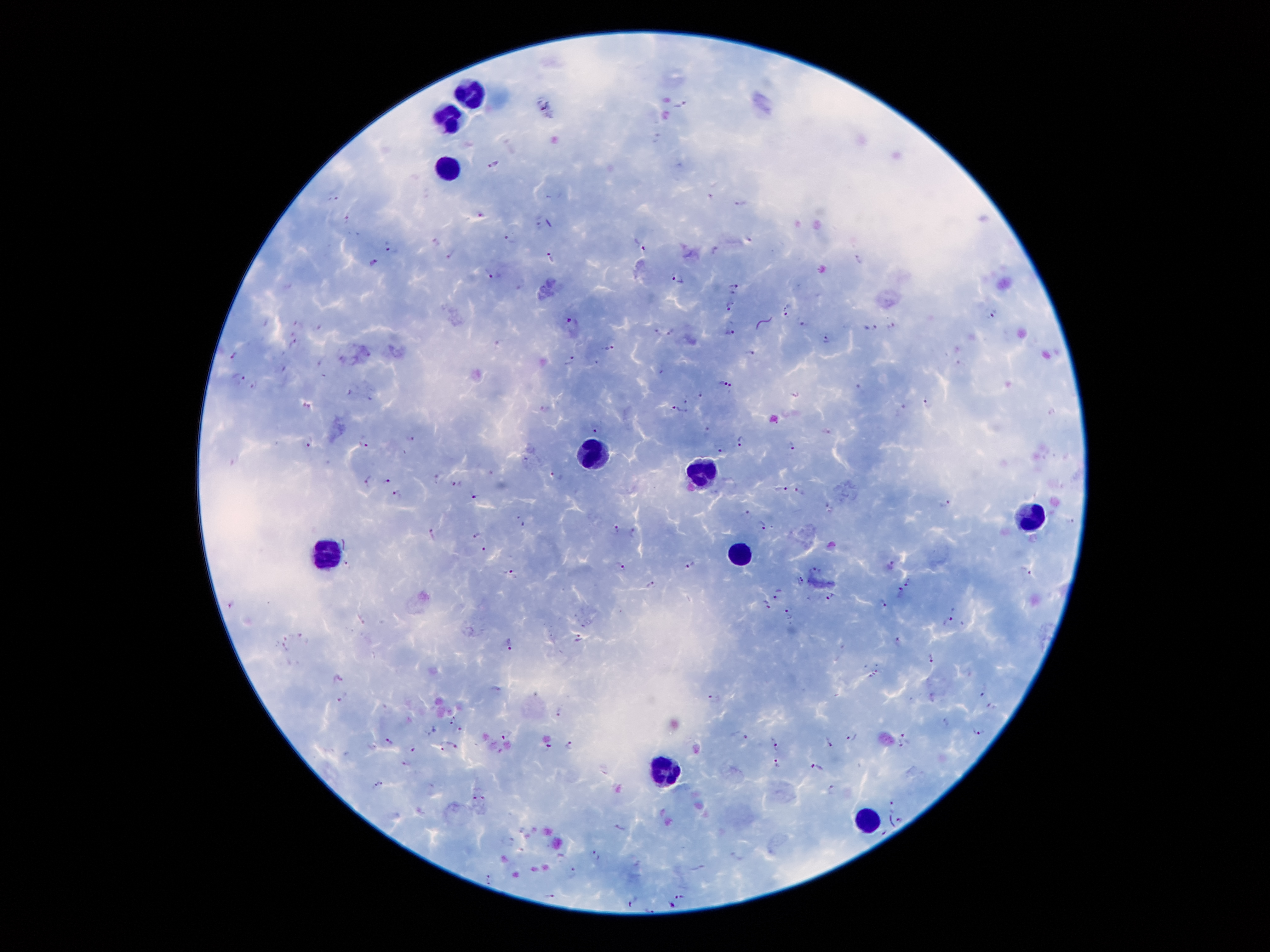

{
  "field_of_view": "one from this slide",
  "stain": "Giemsa",
  "leukocyte_locations": "approximate centers as {x, y} in pixels: {468, 90}, {447, 120}, {447, 166}, {593, 454}, {703, 471}, {1035, 516}, {321, 552}, {738, 555}, {661, 770}, {867, 816}",
  "image_size": "1270×952 pixels",
  "capture": "smartphone camera through the microscope eyepiece",
  "preparation": "thick peripheral-blood smear",
  "patient_malaria_status": "infected with Plasmodium falciparum",
  "plasmodium_parasite_locations": "approximate centers as {x, y} in pixels: {681, 104}, {656, 137}, {492, 162}, {709, 194}, {334, 197}, {739, 201}, {482, 215}, {349, 218}, {538, 221}, {510, 237}, {390, 243}, {640, 243}, {716, 249}, {450, 253}, {550, 257}, {859, 260}, {375, 262}, {491, 273}, {678, 278}, {733, 287}, {730, 304}, {785, 309}, {992, 315}, {572, 322}, {802, 322}, {891, 325}, {869, 326}, {319, 328}, {671, 331}, {730, 332}, {827, 337}, {499, 342}, {294, 343}, {607, 347}, {748, 352}, {233, 355}, {572, 359}, {322, 362}, {241, 379}, {724, 382}, {861, 386}, {701, 395}, {372, 398}, {685, 400}, {926, 403}, {546, 409}, {675, 409}, {902, 409}, {598, 427}, {707, 430}, {414, 437}, {309, 441}, {740, 441}, {364, 444}, {792, 445}, {719, 448}, {527, 458}, {556, 474}, {367, 479}, {386, 479}, {456, 484}, {780, 488}, {799, 490}, {396, 493}, {473, 496}, {947, 504}, {748, 514}, {521, 521}, {1072, 523}, {765, 525}, {618, 527}, {432, 532}, {635, 534}, {474, 536}, {484, 548}, {349, 563}, {690, 563}, {620, 567}, {892, 567}, {510, 571}, {814, 571}, {1027, 571}, {800, 579}, {907, 584}, {650, 585}, {778, 592}, {900, 593}, {830, 595}, {767, 604}, {230, 605}, {882, 605}, {788, 610}, {949, 620}, {585, 623}, {303, 637}, {580, 639}, {898, 640}, {510, 643}, {284, 645}, {931, 658}, {877, 670}, {871, 676}, {340, 679}, {984, 693}, {343, 696}, {715, 699}, {993, 707}, {559, 712}, {454, 721}, {435, 730}, {980, 730}, {459, 731}, {904, 733}, {739, 735}, {504, 736}, {853, 737}, {389, 740}, {829, 742}, {776, 744}, {570, 745}, {453, 746}, {549, 746}, {902, 746}, {442, 747}, {411, 749}, {407, 765}, {776, 767}, {816, 768}, {382, 779}, {375, 786}, {831, 789}, {485, 794}, {474, 795}, {893, 804}, {901, 817}, {621, 826}, {510, 840}, {595, 855}, {738, 857}, {561, 858}, {699, 868}, {573, 873}, {488, 879}, {683, 895}, {550, 896}, {633, 902}, {671, 904}",
  "magnification": "100x"
}